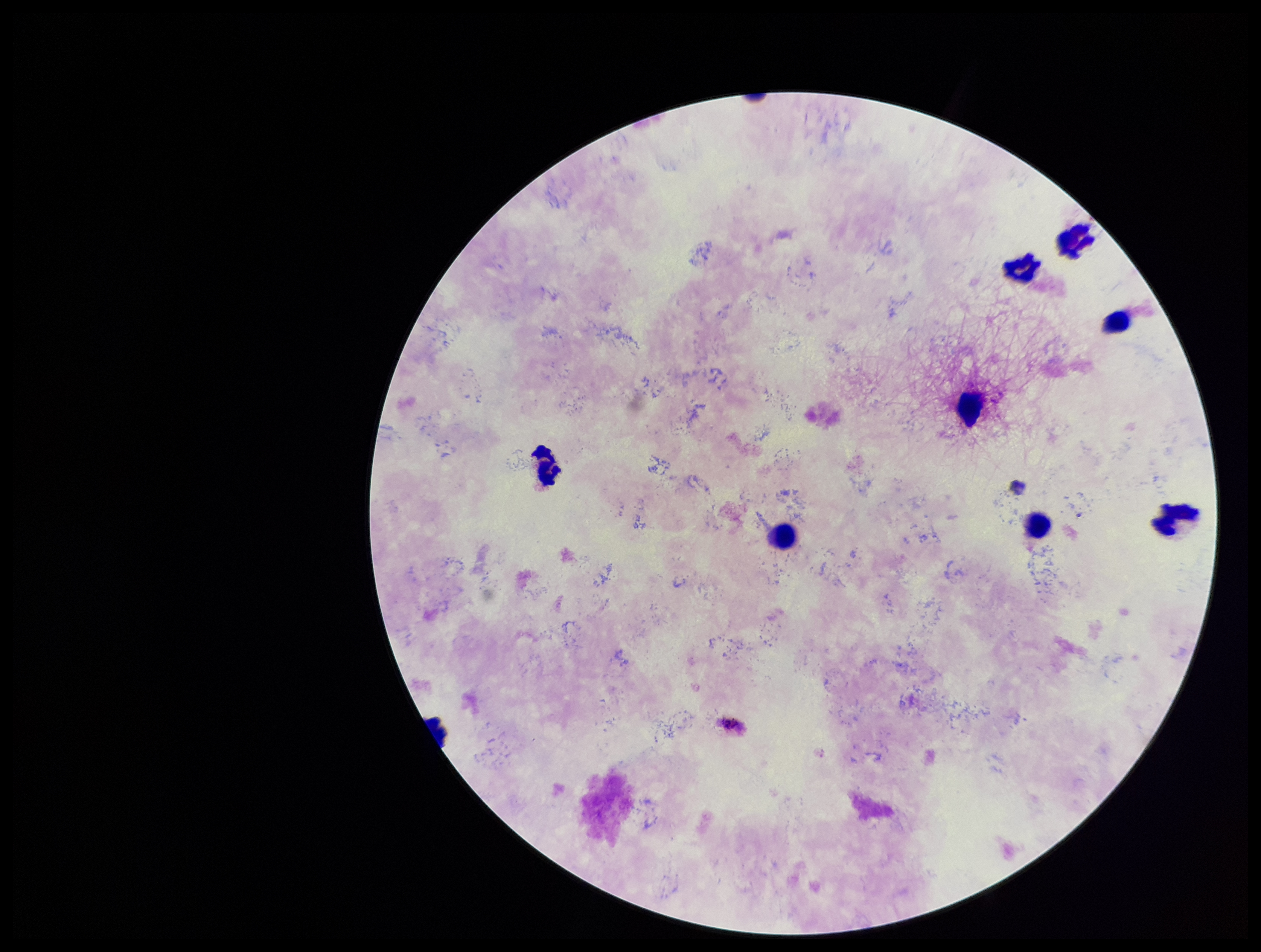

stain = Giemsa
capture = smartphone photograph through the microscope eyepiece
image size = 1261×952 pixels
patient malaria status = positive
field of view = single
preparation = thick
leukocyte count = 8
Plasmodium parasites = none detected
species reported for this patient = Plasmodium falciparum
parasite count = 0